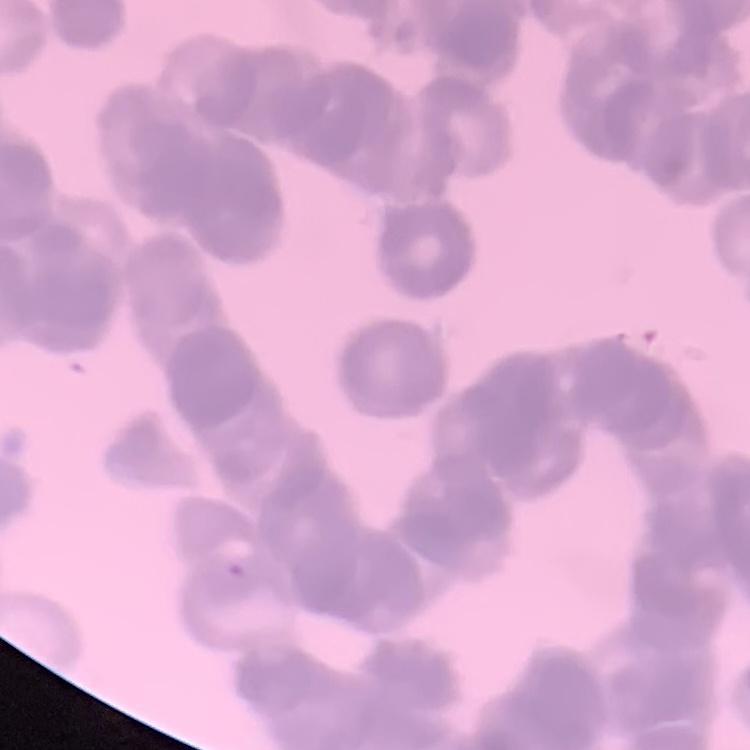
erythrocyte morphology = rouleaux formation
image type = one tile cut from a larger photomicrograph
stain = Field's or Giemsa
preparation = thin peripheral smear